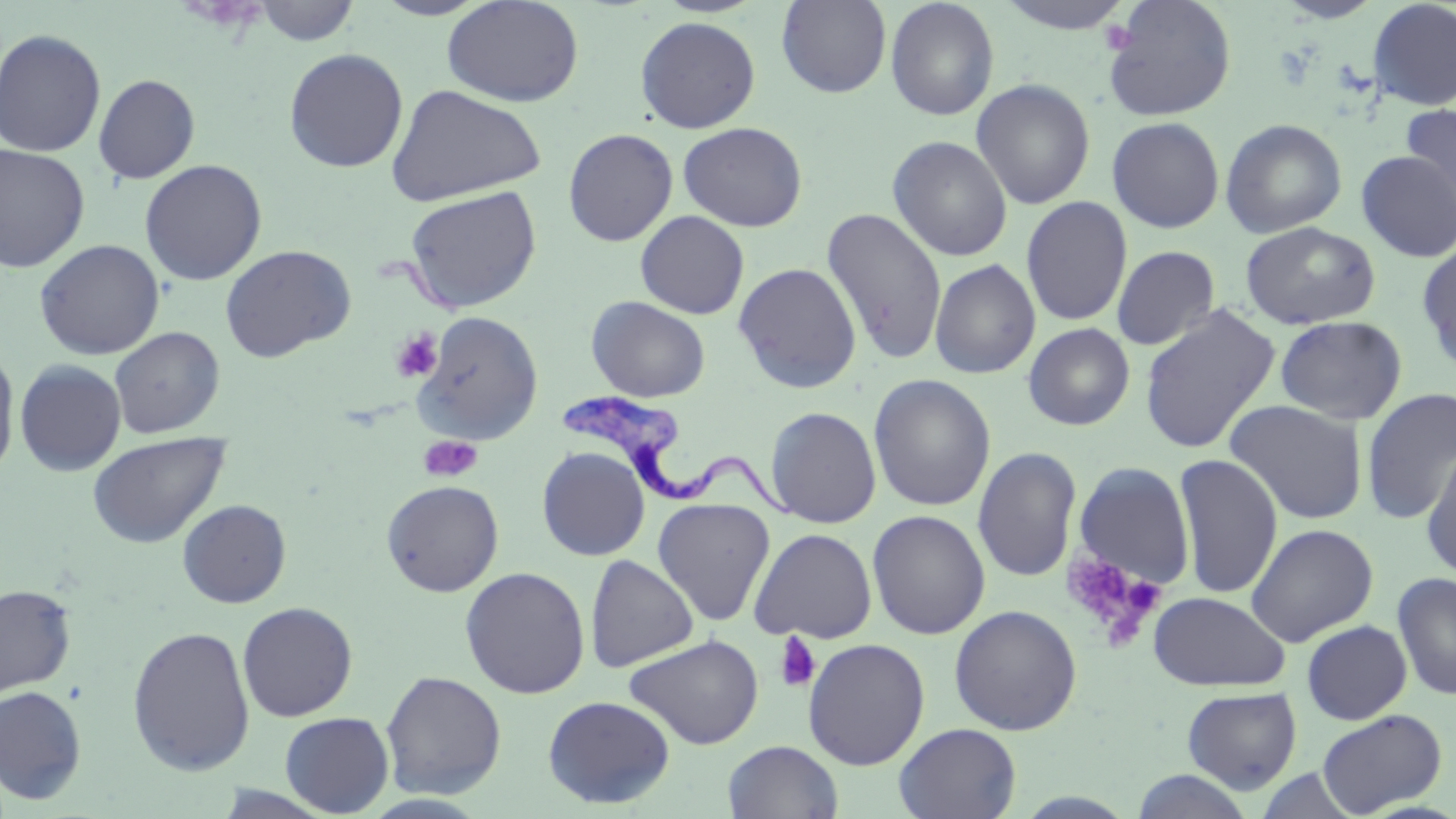
{
  "trypanosoma_brucei_locations": "approximate bounding boxes as (x1, y1, x2, y2) in pixels: (558, 392, 802, 521)",
  "slide_level_diagnosis": "Trypanosoma brucei",
  "image_size": "1456×819 pixels",
  "stain": "May-Grünwald-Giemsa",
  "platelet_locations": "approximate bounding boxes as (x1, y1, x2, y2) in pixels: (1102, 19, 1138, 52), (391, 329, 444, 382), (419, 434, 483, 482), (1060, 551, 1161, 639), (774, 631, 821, 693)",
  "modality": "light microscopy",
  "uninfected_red_blood_cell_locations": "approximate bounding boxes as (x1, y1, x2, y2) in pixels: (370, 0, 495, 20), (442, 0, 585, 107), (776, 0, 892, 98), (884, 0, 1000, 121), (992, 0, 1141, 35), (1102, 0, 1238, 122), (1367, 0, 1456, 111), (250, 1, 361, 46), (634, 16, 761, 133), (0, 28, 106, 158), (283, 48, 408, 173), (93, 74, 200, 184), (971, 78, 1096, 210), (386, 83, 546, 207), (1400, 104, 1456, 218), (1107, 116, 1225, 233), (1220, 118, 1348, 238), (677, 121, 809, 231), (562, 128, 679, 246), (887, 135, 1013, 261), (0, 144, 91, 273), (1356, 151, 1456, 262), (139, 159, 267, 285), (404, 185, 542, 313), (1021, 196, 1133, 327), (821, 206, 948, 365), (635, 210, 749, 319), (1239, 222, 1380, 330), (35, 239, 164, 360), (1416, 241, 1456, 375), (220, 244, 356, 362), (1111, 245, 1220, 350), (929, 258, 1041, 379), (733, 262, 863, 394), (586, 296, 711, 402), (1139, 304, 1281, 454), (414, 311, 544, 444), (1275, 315, 1407, 425), (1022, 323, 1136, 431), (109, 327, 225, 438), (0, 344, 20, 480), (14, 359, 126, 476), (868, 374, 996, 511), (1361, 387, 1456, 525), (1224, 399, 1369, 524), (765, 406, 882, 528), (87, 431, 229, 548), (1421, 440, 1456, 584), (972, 446, 1082, 583), (537, 447, 650, 561), (1173, 452, 1284, 599), (1071, 460, 1198, 594), (381, 479, 504, 597), (652, 497, 776, 626), (177, 498, 291, 608), (867, 509, 991, 640), (1245, 523, 1379, 647), (748, 527, 878, 644), (584, 554, 699, 672), (459, 566, 591, 699), (1393, 571, 1456, 701), (0, 583, 76, 700), (1148, 590, 1290, 692), (236, 601, 358, 722), (948, 604, 1083, 735), (1302, 619, 1413, 725), (127, 624, 255, 777), (624, 633, 764, 750), (803, 638, 930, 770), (380, 670, 507, 799), (0, 685, 87, 805), (1181, 686, 1303, 794), (542, 695, 675, 809), (1317, 708, 1447, 816), (279, 712, 394, 817), (894, 722, 1022, 819), (723, 740, 844, 819), (1129, 769, 1257, 818)",
  "magnification": "1000x",
  "field_of_view": "one of a larger specimen",
  "preparation": "thin blood film"
}